Assess this cell for malaria.
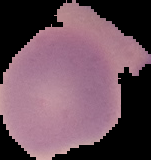

It is uninfected.

Summary:
  - Preparation: thin blood film
  - Image size: 151×160 pixels
  - Image type: cell region segmented out of the field of view; surrounding area masked to black